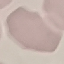

Result: no malaria parasites seen. Thin smear of blood. Cell patch, automatically extracted from a larger field of view and resized to 64 × 64 pixels. Giemsa stain. Photographed with a smartphone camera at the microscope eyepiece.